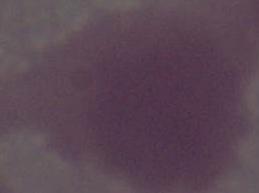

modality = micrograph
identification = red blood cell
magnification = 1000x